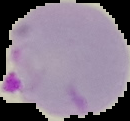
image type = segmented cell region on a black background
image size = 130×121 pixels
preparation = thin blood smear
malaria status = parasitized